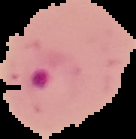

result: malaria parasites identified
image_type: cell region segmented out of the field of view; surrounding area masked to black
preparation: thin blood film
image_size: 136×139 pixels